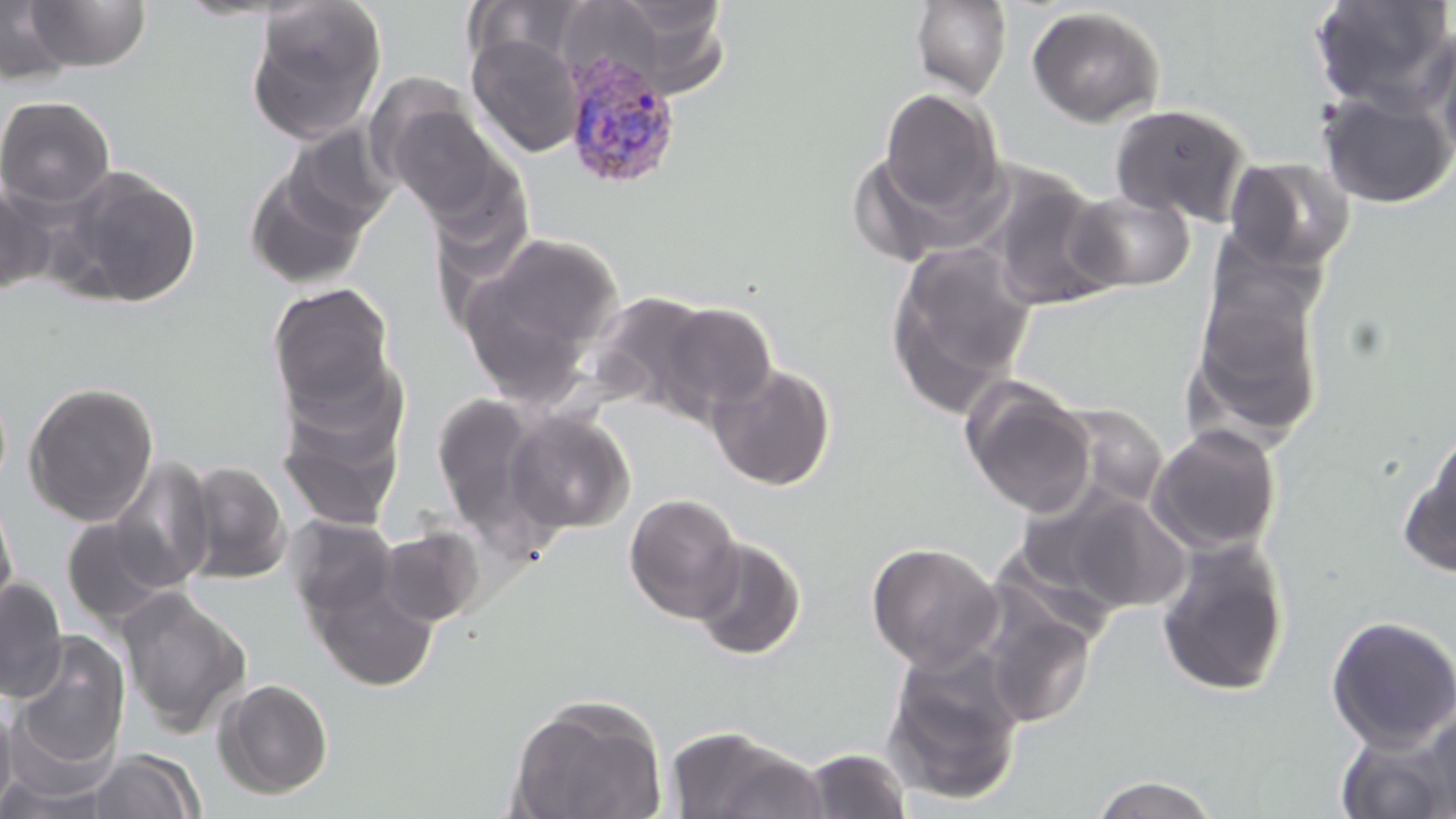

slide_level_diagnosis: Plasmodium vivax
magnification: 1000x
plasmodium_vivax_infected_red_blood_cell_locations: 'approximate bounding boxes as (x1,y1)-(x2,y2) corner pairs in pixels: (562,49)-(681,190)'
image_size: 1456×819 pixels
preparation: thin blood film
field_of_view: one of a larger specimen
uninfected_red_blood_cell_locations: 'approximate bounding boxes as (x1,y1)-(x2,y2) corner pairs in pixels: (24,0)-(153,72), (1310,0)-(1456,114), (0,1)-(77,85), (247,1)-(388,143), (910,1)-(1012,100), (1026,6)-(1165,127), (1433,25)-(1456,167), (467,34)-(584,157), (878,88)-(1003,220), (1317,89)-(1456,209), (0,95)-(116,209), (381,99)-(511,223), (1109,103)-(1253,226), (1224,157)-(1354,272), (58,168)-(202,307), (245,168)-(370,291), (980,168)-(1122,313), (0,185)-(57,296), (1067,190)-(1196,292), (457,230)-(626,395), (886,241)-(1038,413), (1189,274)-(1327,444), (267,282)-(397,418), (657,302)-(778,418), (707,362)-(836,491), (276,373)-(409,532), (23,380)-(160,527), (963,382)-(1097,518), (430,391)-(546,529), (503,409)-(635,534), (1146,423)-(1282,555), (1400,430)-(1456,579), (107,457)-(217,591), (180,460)-(292,584), (0,490)-(18,624), (1057,491)-(1192,614), (623,492)-(744,623), (287,515)-(399,621), (61,516)-(180,627), (377,525)-(485,627), (1154,535)-(1292,698), (691,536)-(807,661), (866,540)-(1004,672), (0,577)-(68,702), (311,578)-(439,691), (116,587)-(253,736), (980,604)-(1098,729), (1324,614)-(1456,752), (10,631)-(131,770), (881,649)-(1026,808), (213,678)-(335,800), (506,694)-(668,819), (0,698)-(18,815), (1420,708)-(1456,815), (663,726)-(825,819), (1334,729)-(1455,819), (797,748)-(914,819), (86,749)-(203,818), (0,773)-(122,818), (1088,774)-(1222,818)'
stain: May-Grünwald-Giemsa
modality: light microscopy